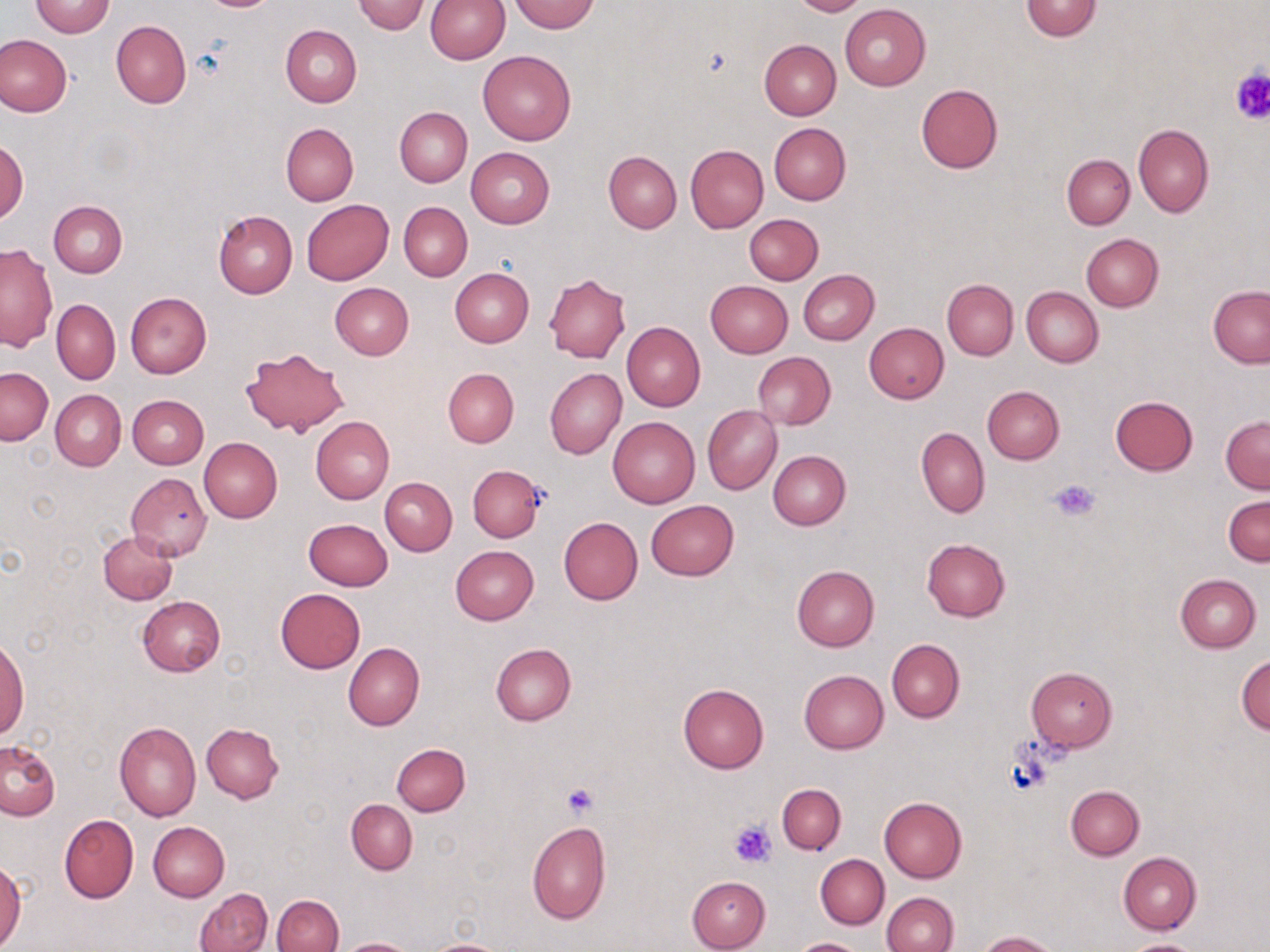 Approximate bounding boxes as (x1, y1, x2, y2) in pixels. Uninfected red blood cell locations: (424, 0, 510, 63), (511, 0, 599, 33), (790, 0, 867, 16), (30, 1, 115, 37), (352, 1, 431, 34), (1021, 1, 1101, 41), (840, 3, 931, 89), (111, 20, 191, 109), (281, 25, 361, 108), (0, 34, 73, 116), (758, 39, 841, 120), (478, 50, 576, 144), (916, 83, 1002, 174), (395, 107, 472, 187), (281, 122, 358, 206), (769, 122, 851, 204), (1132, 124, 1213, 218), (0, 137, 28, 224), (685, 145, 768, 232), (466, 147, 555, 227), (603, 151, 682, 234), (1062, 154, 1134, 229), (301, 200, 394, 286), (49, 201, 127, 278), (400, 203, 472, 281), (214, 210, 297, 298), (743, 213, 823, 285), (1081, 234, 1163, 312), (0, 243, 57, 352), (449, 269, 534, 347), (798, 269, 879, 344), (543, 273, 631, 362), (942, 279, 1018, 360), (706, 280, 793, 356), (329, 282, 413, 360), (1208, 285, 1270, 369), (1022, 287, 1103, 367), (126, 292, 212, 378), (52, 300, 120, 384), (622, 322, 705, 413), (864, 322, 949, 403), (240, 347, 350, 437), (753, 352, 836, 430), (1, 368, 53, 445), (442, 368, 518, 447), (545, 368, 626, 459), (982, 385, 1064, 463), (51, 390, 126, 471), (128, 394, 209, 469), (1110, 396, 1198, 476), (702, 406, 781, 495), (608, 416, 699, 508), (1220, 416, 1270, 493), (311, 417, 394, 504), (916, 427, 989, 518), (199, 437, 282, 523), (767, 450, 851, 530), (466, 464, 545, 542), (125, 472, 211, 562), (379, 477, 456, 555), (1224, 494, 1269, 567), (646, 500, 739, 579), (558, 517, 642, 605), (304, 518, 392, 591), (98, 530, 178, 604), (921, 539, 1010, 622), (450, 545, 539, 625), (792, 565, 879, 651), (1176, 574, 1260, 652), (275, 588, 366, 673), (137, 595, 226, 676), (0, 637, 29, 742), (886, 638, 965, 723), (343, 642, 424, 730), (490, 643, 576, 725), (1235, 652, 1270, 735), (1026, 666, 1118, 752), (799, 669, 889, 753), (677, 683, 769, 774), (114, 722, 201, 821), (202, 723, 284, 803), (0, 741, 60, 820), (392, 743, 470, 816), (777, 783, 846, 854), (1066, 785, 1145, 859), (879, 796, 967, 882), (347, 800, 417, 873), (59, 814, 138, 903), (149, 821, 229, 902), (526, 822, 611, 925), (1118, 852, 1201, 935), (816, 855, 889, 929), (0, 861, 26, 948), (687, 876, 770, 951), (195, 888, 273, 952), (881, 892, 957, 952), (273, 894, 343, 952), (978, 931, 1060, 952), (336, 938, 419, 952), (420, 938, 510, 952), (1121, 938, 1205, 952), (792, 939, 863, 952). Platelet locations: (1229, 67, 1270, 122), (1050, 478, 1101, 522), (560, 783, 600, 820), (727, 821, 777, 868). Slide-level diagnosis: negative for blood parasites. One field of a larger specimen. Image is 1270×952 pixels. Thin blood smear. May-Grünwald-Giemsa-stained preparation. Captured at 1000x magnification. Optical microscopy.